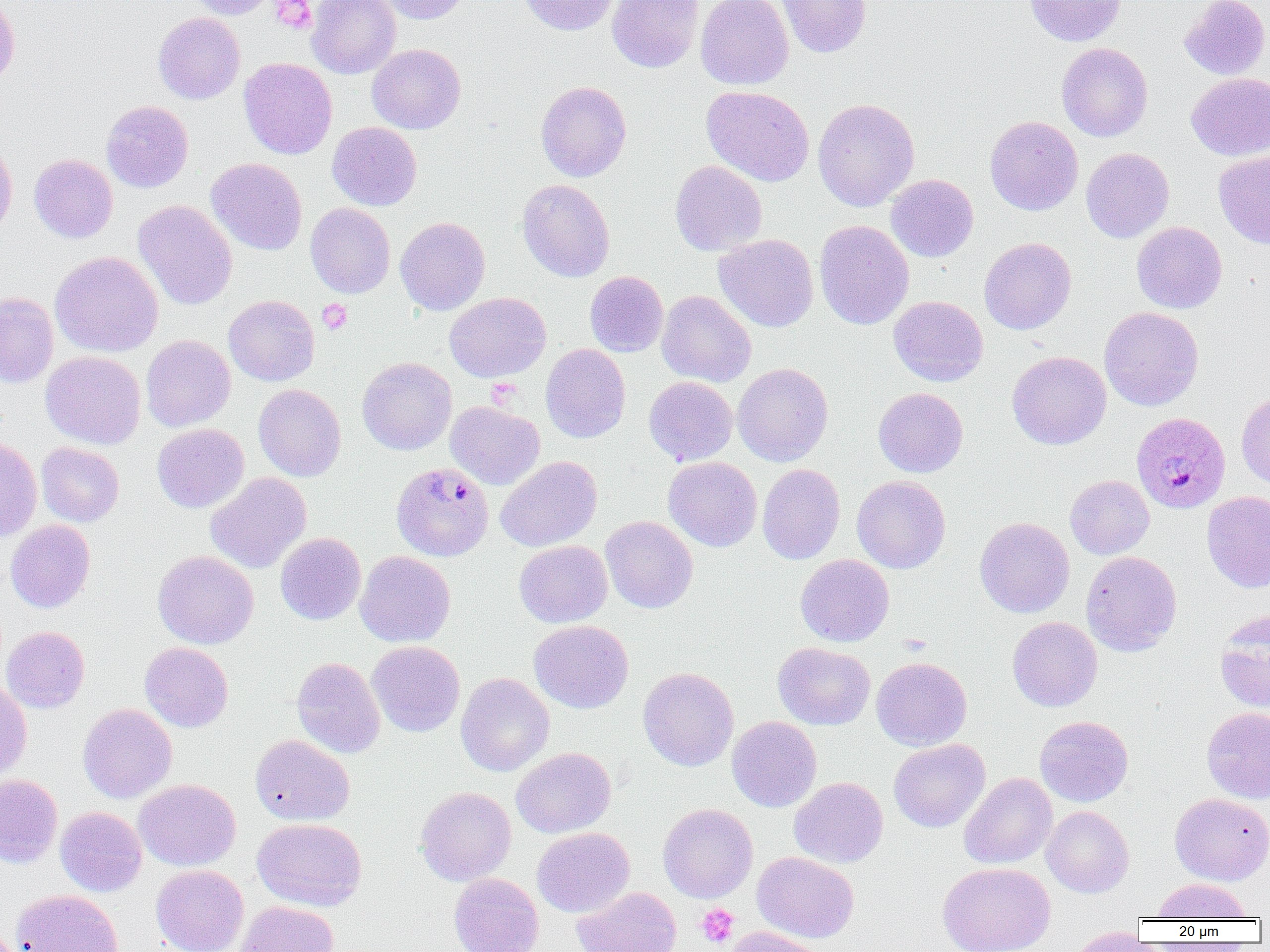
{
  "slide_level_diagnosis": "Plasmodium malariae",
  "image_size": "1270×952 pixels",
  "magnification": "1000x",
  "modality": "optical microscopy",
  "plasmodium_malariae_infected_red_blood_cell_locations": "approximate bounding boxes as (x1,y1)-(x2,y2) corner pairs in pixels: (1131,412)-(1230,514), (391,462)-(494,561)",
  "field_of_view": "one of a larger specimen",
  "platelet_locations": "approximate bounding boxes as (x1,y1)-(x2,y2) corner pairs in pixels: (270,0)-(317,33), (317,299)-(353,334), (486,379)-(521,407), (697,903)-(739,948)",
  "uninfected_red_blood_cell_locations": "approximate bounding boxes as (x1,y1)-(x2,y2) corner pairs in pixels: (0,0)-(20,88), (183,0)-(277,20), (306,0)-(401,79), (375,0)-(473,24), (518,0)-(621,35), (607,0)-(703,73), (696,0)-(793,90), (776,0)-(872,58), (1024,0)-(1127,46), (1179,0)-(1270,80), (153,12)-(245,104), (1057,42)-(1153,142), (367,43)-(466,134), (239,58)-(337,159), (1186,72)-(1270,160), (535,81)-(631,182), (702,86)-(814,186), (812,98)-(919,211), (101,100)-(193,192), (984,115)-(1083,216), (327,122)-(422,210), (0,137)-(17,239), (1081,148)-(1174,243), (1214,151)-(1270,248), (29,154)-(118,243), (206,158)-(307,255), (670,160)-(767,256), (886,174)-(978,262), (517,179)-(615,282), (133,200)-(237,311), (305,202)-(395,298), (395,216)-(490,315), (814,220)-(914,330), (1131,222)-(1227,314), (713,234)-(819,332), (979,237)-(1077,335), (50,251)-(163,358), (585,271)-(668,357), (657,290)-(756,387), (0,292)-(58,388), (444,292)-(551,382), (223,294)-(319,386), (889,295)-(988,387), (1099,306)-(1204,411), (141,335)-(235,431), (541,343)-(631,443), (1007,350)-(1111,449), (41,351)-(146,449), (357,357)-(457,455), (732,362)-(833,466), (644,376)-(738,466), (253,384)-(346,481), (873,387)-(968,478), (1236,389)-(1270,490), (445,401)-(545,489), (152,423)-(249,512), (0,435)-(42,542), (36,442)-(124,527), (496,455)-(602,552), (663,457)-(762,551), (757,463)-(845,564), (205,472)-(311,573), (852,475)-(950,573), (1065,475)-(1154,560), (1202,491)-(1270,593), (600,516)-(698,613), (974,516)-(1075,618), (5,519)-(95,613), (275,532)-(366,625), (514,540)-(612,627), (152,550)-(259,649), (355,550)-(455,648), (1081,551)-(1182,656), (795,554)-(894,647), (1216,612)-(1270,713), (1007,616)-(1102,711), (529,620)-(633,713), (1,626)-(90,713), (367,641)-(465,736), (139,642)-(233,732), (773,642)-(875,730), (291,657)-(386,758), (871,657)-(972,751), (638,667)-(739,771), (455,672)-(554,776), (0,679)-(32,780), (78,703)-(177,804), (1201,706)-(1270,804), (727,716)-(822,812), (1034,716)-(1133,806), (250,734)-(355,825), (888,739)-(990,832), (511,747)-(615,838), (959,772)-(1057,869), (0,774)-(62,868), (789,777)-(888,868), (134,779)-(241,871), (416,786)-(516,886), (1169,792)-(1270,885), (658,803)-(758,903), (1041,805)-(1134,897), (55,806)-(147,896), (252,818)-(366,911), (532,827)-(634,917), (752,851)-(859,943), (938,862)-(1055,952), (151,865)-(248,952), (449,873)-(544,952), (1152,877)-(1252,920), (573,886)-(682,952), (11,889)-(124,952), (235,901)-(339,952), (722,926)-(827,952), (1066,927)-(1156,951)",
  "preparation": "thin blood film"
}